Name the parasite shown.
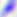

Toxoplasma gondii.

modality = micrograph
magnification = 400x